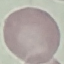
Summary:
  - Result: no malaria parasites seen
  - Stain: Giemsa
  - Image type: cell patch, automatically extracted from a larger field of view and resized to 64 × 64 pixels
  - Preparation: thin blood film
  - Capture: smartphone camera at the microscope eyepiece